Classify this cell by malaria status.
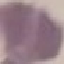

Uninfected.

Giemsa-stained preparation. Acquired by smartphone through the microscope eyepiece. Thin blood smear. Cell patch, automatically extracted from a larger field of view and resized to 64 × 64 pixels.